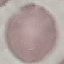
Summary:
  - Result: no malaria parasites detected
  - Preparation: thin blood film
  - Stain: Giemsa
  - Capture: smartphone through the microscope eyepiece
  - Image type: cell patch, automatically extracted from a larger field of view and resized to 64 × 64 pixels